Assess this cell for malaria.
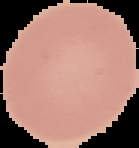

It is uninfected.

image size = 139×148 pixels
preparation = thin blood film
image type = segmented cell region on a black background